Name the cell type shown.
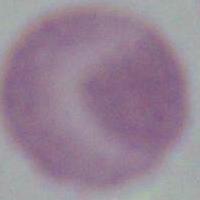

This is an erythrocyte.

magnification = 1000x
modality = photomicrograph